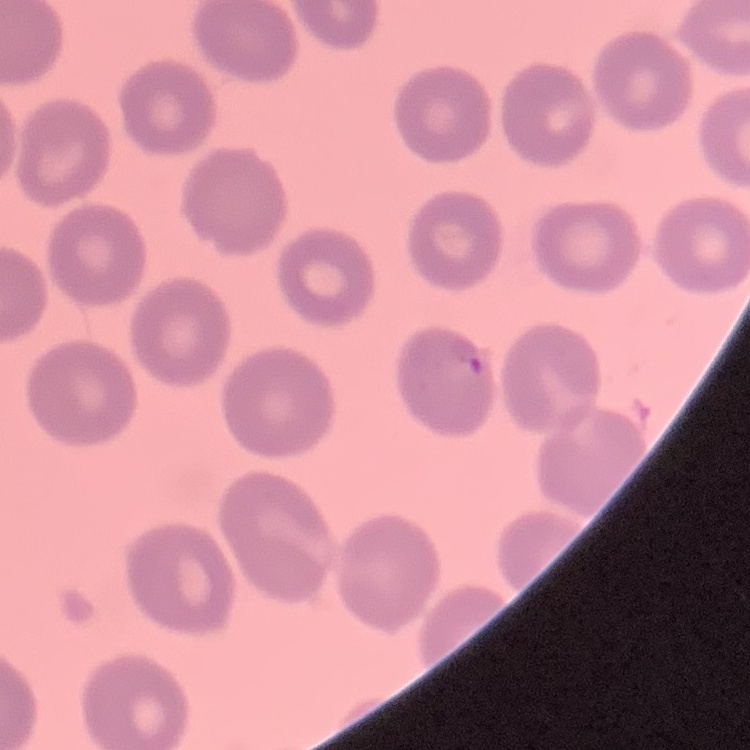
The red blood cells exhibit no rouleaux formation. Thin blood smear. Field's or Giemsa stain. Square crop of a larger photomicrograph.